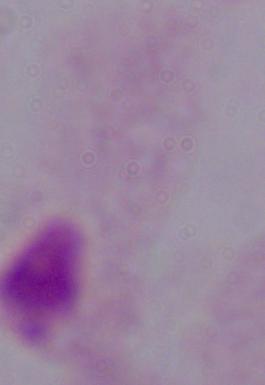
A trichomonad is seen. Photomicrograph. 1000x magnification.